Locate every Plasmodium parasite.
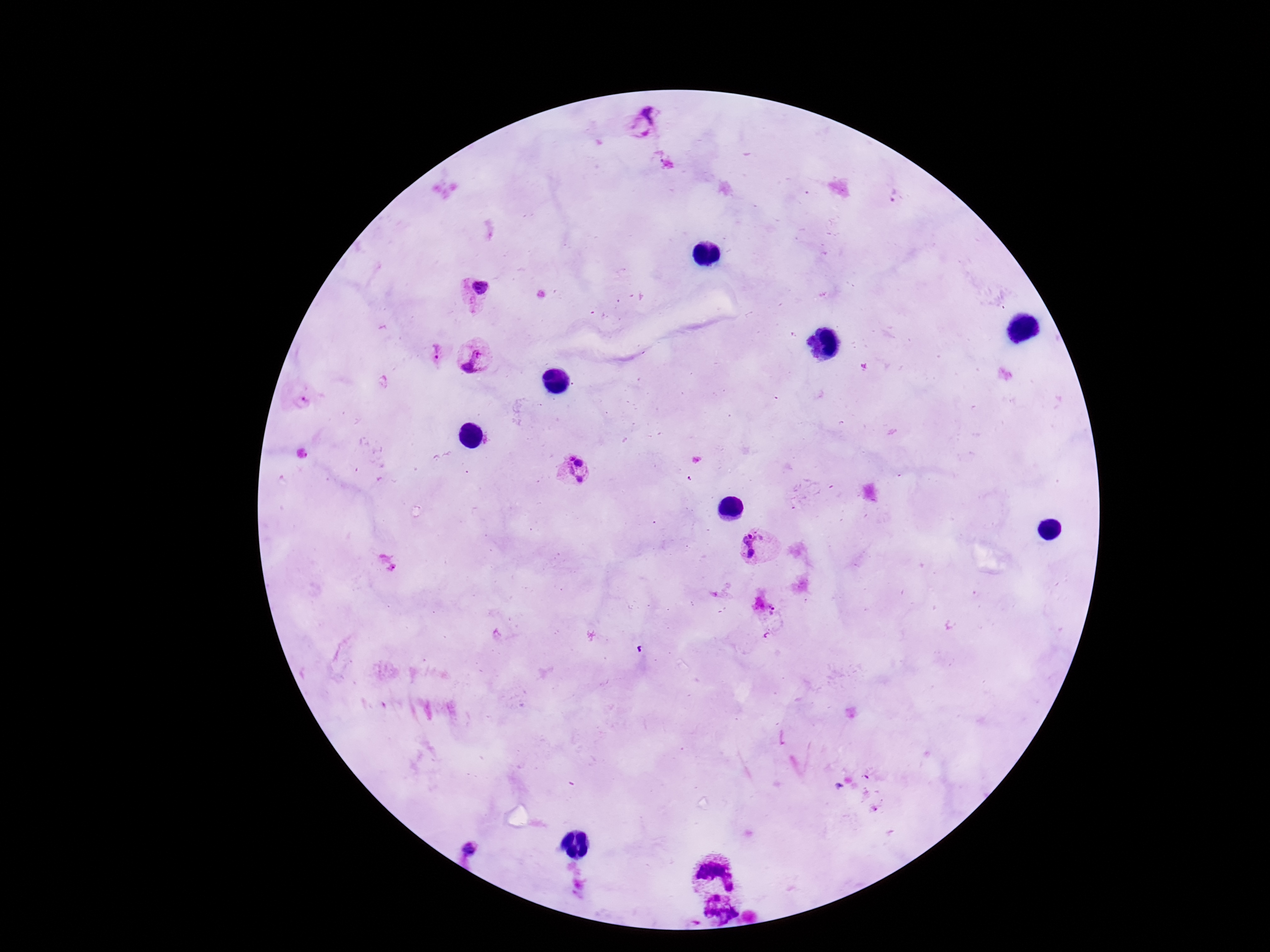

Approximate object centers, in pixels from the top-left corner.
Plasmodium parasites: (x=647, y=125), (x=892, y=196), (x=476, y=294), (x=433, y=353), (x=476, y=357), (x=303, y=402), (x=573, y=472), (x=759, y=545), (x=773, y=616), (x=470, y=849), (x=715, y=871), (x=720, y=910).

Summary:
  - Field of view: one from this slide
  - Patient malaria status: positive
  - Magnification: 100x
  - Preparation: thick blood smear
  - Capture: smartphone camera through the microscope eyepiece
  - Image size: 1270×952 pixels
  - Stain: Giemsa